Give the extent of all uninfected red blood cells.
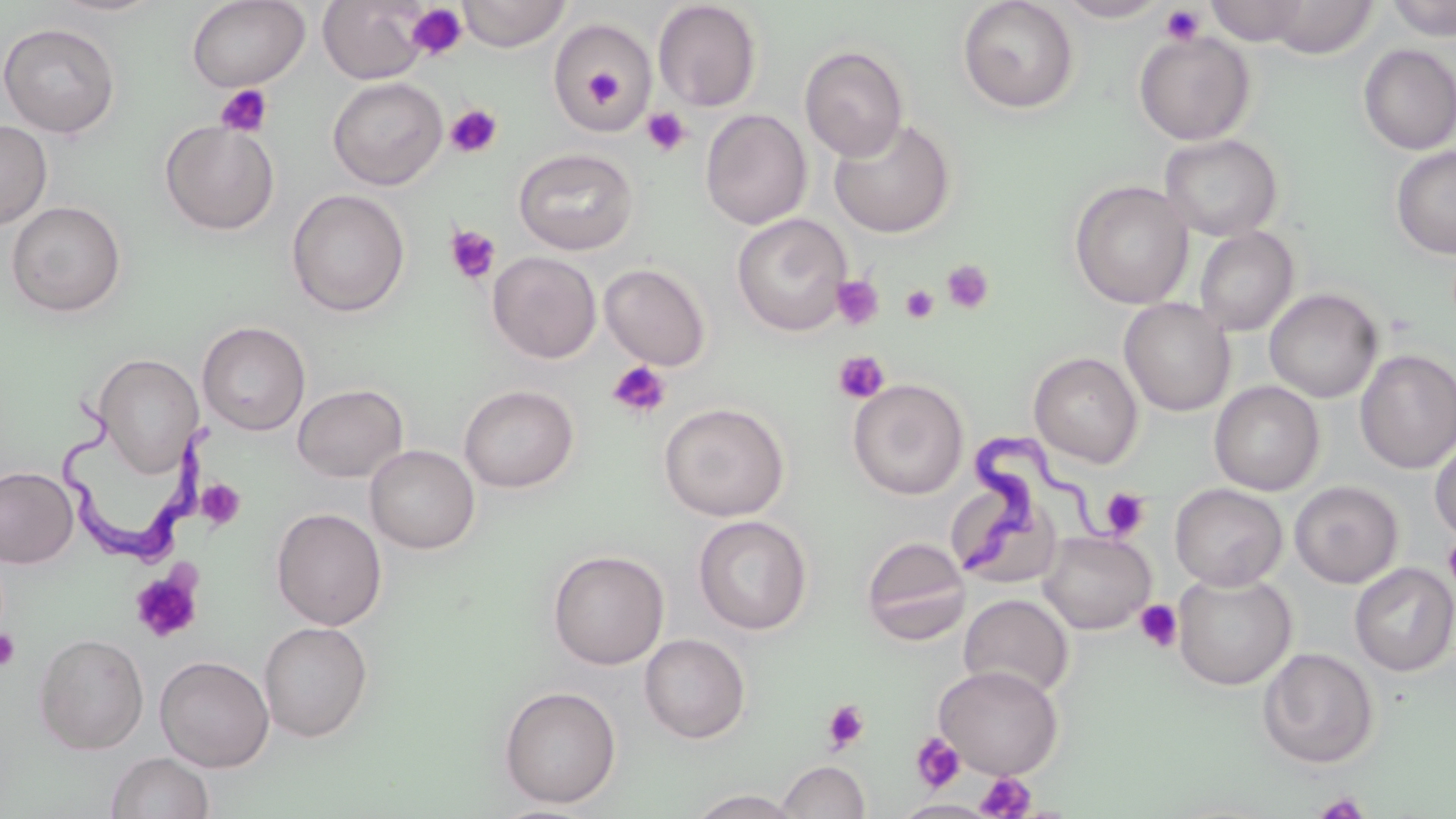

Approximate bounding boxes as (x1,y1)-(x2,y2) corner pairs in pixels.
Uninfected red blood cells: (186,0)-(310,92), (318,0)-(430,84), (456,0)-(572,52), (957,0)-(1079,115), (1055,0)-(1171,23), (1204,0)-(1313,44), (1385,0)-(1456,41), (47,1)-(167,18), (652,1)-(763,112), (1256,1)-(1381,58), (549,17)-(656,133), (0,22)-(121,138), (1134,30)-(1255,145), (799,45)-(909,162), (1357,45)-(1456,155), (327,76)-(448,190), (700,109)-(812,230), (828,117)-(956,238), (0,119)-(52,229), (159,119)-(280,236), (1159,133)-(1283,241), (1391,146)-(1456,259), (513,147)-(639,255), (1069,179)-(1193,309), (286,189)-(410,317), (6,200)-(127,317), (731,213)-(851,336), (1194,226)-(1299,337), (487,251)-(601,363), (599,262)-(712,370), (1264,288)-(1382,403), (1119,298)-(1236,416), (197,321)-(310,435), (1354,349)-(1456,474), (1029,352)-(1143,468), (94,353)-(203,477), (847,378)-(969,500), (1209,381)-(1325,495), (292,383)-(408,483), (459,384)-(579,493), (658,402)-(790,522), (1429,433)-(1456,544), (365,444)-(480,554), (0,466)-(78,568), (1289,480)-(1403,588), (1170,483)-(1288,590), (271,507)-(387,630), (693,515)-(812,635), (1038,531)-(1156,635), (861,535)-(971,645), (548,549)-(669,670), (1349,562)-(1456,677), (1173,572)-(1297,690), (958,593)-(1074,700), (258,620)-(373,742), (33,632)-(149,754), (639,633)-(751,744), (1257,647)-(1380,769), (155,655)-(275,772), (933,664)-(1064,779), (498,685)-(622,809), (106,750)-(215,819), (777,760)-(871,819), (689,788)-(803,818), (894,800)-(995,818).

Trypanosoma brucei locations = approximate bounding boxes as (x1,y1)-(x2,y2) corner pairs in pixels: (59,381)-(214,574), (946,432)-(1109,580)
slide-level diagnosis = Trypanosoma brucei
modality = light microscopy
image size = 1456×819 pixels
stain = May-Grünwald-Giemsa
preparation = thin blood film
field of view = single
magnification = 1000x
platelet locations = approximate bounding boxes as (x1,y1)-(x2,y2) corner pairs in pixels: (406,4)-(468,60), (1160,4)-(1205,46), (578,53)-(628,113), (214,84)-(273,138), (445,104)-(503,158), (641,107)-(690,157), (444,225)-(501,284), (941,260)-(995,314), (831,274)-(884,331), (899,284)-(940,324), (832,350)-(891,404), (606,360)-(672,419), (196,478)-(246,529), (1101,488)-(1150,539), (1443,535)-(1456,593), (130,568)-(203,643), (1134,599)-(1183,653), (0,629)-(21,671), (821,699)-(870,754), (910,732)-(966,793), (976,771)-(1035,818), (1311,792)-(1372,818)